Locate every blood parasite and identify its species.
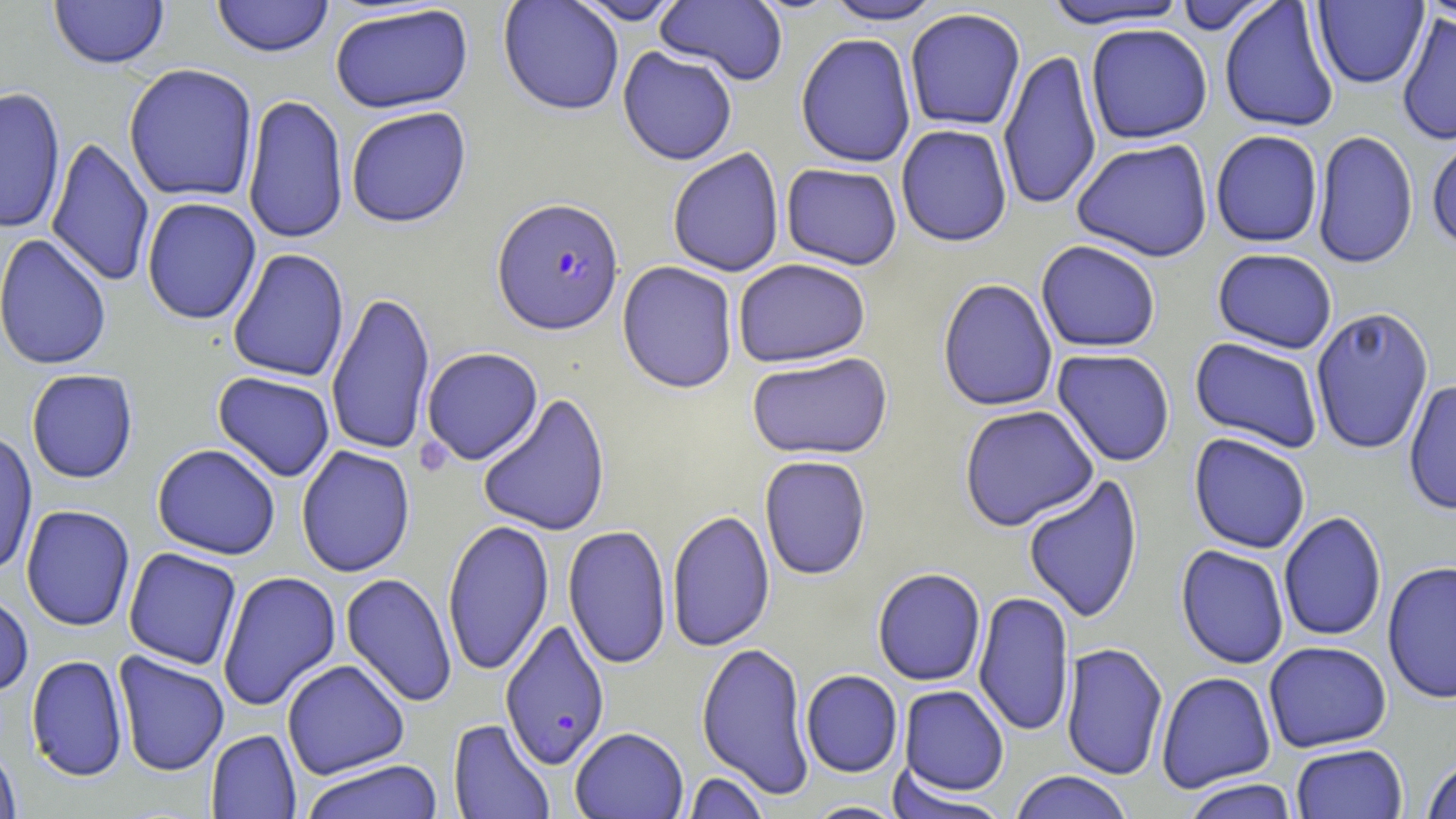
Approximate bounding boxes as (x1,y1)-(x2,y2) corner pairs in pixels.
Plasmodium falciparum-infected red blood cells: (492,196)-(624,336), (499,619)-(611,770).
No Plasmodium ovale, Plasmodium malariae, Plasmodium vivax, Babesia divergens, or Trypanosoma brucei observed.

slide-level diagnosis = Plasmodium falciparum
field of view = single
modality = optical microscopy
platelet locations = approximate bounding boxes as (x1,y1)-(x2,y2) corner pairs in pixels: (414,436)-(454,477)
stain = May-Grünwald-Giemsa
image size = 1456×819 pixels
uninfected red blood cell locations = approximate bounding boxes as (x1,y1)-(x2,y2) corner pairs in pixels: (48,0)-(170,70), (210,0)-(335,58), (498,0)-(624,116), (567,0)-(688,25), (655,0)-(790,86), (822,0)-(945,25), (1171,0)-(1280,34), (1417,0)-(1455,26), (1038,1)-(1191,30), (1219,1)-(1340,133), (1312,1)-(1429,89), (329,5)-(474,114), (904,8)-(1026,132), (1396,12)-(1456,146), (1085,23)-(1213,144), (795,32)-(917,168), (617,46)-(738,166), (998,48)-(1101,212), (123,63)-(258,204), (0,85)-(67,235), (242,94)-(349,245), (345,106)-(472,228), (896,124)-(1012,247), (1312,129)-(1419,269), (1210,130)-(1323,248), (1426,135)-(1456,250), (46,136)-(154,288), (1071,138)-(1213,263), (667,148)-(785,278), (780,163)-(903,270), (141,197)-(262,325), (0,233)-(113,370), (1035,240)-(1161,353), (227,248)-(349,382), (1212,248)-(1338,354), (732,258)-(871,368), (616,261)-(739,394), (937,278)-(1058,412), (326,290)-(435,457), (1310,306)-(1435,455), (1189,337)-(1324,453), (420,347)-(543,465), (1052,349)-(1175,467), (746,352)-(894,461), (25,369)-(139,484), (212,371)-(335,482), (1403,379)-(1456,516), (477,393)-(611,537), (959,405)-(1099,531), (0,428)-(38,578), (1188,433)-(1311,554), (152,443)-(281,560), (296,445)-(416,577), (759,455)-(871,580), (1022,474)-(1144,625), (20,505)-(136,632), (667,509)-(775,652), (1278,511)-(1387,642), (442,519)-(554,677), (562,524)-(672,669), (1175,545)-(1290,669), (123,547)-(242,670), (1381,560)-(1456,705), (872,568)-(986,686), (217,571)-(341,711), (340,572)-(458,708), (0,588)-(35,697), (973,591)-(1075,738), (1263,641)-(1392,752), (696,642)-(813,798), (1061,642)-(1169,781), (112,652)-(230,776), (25,654)-(129,782), (282,659)-(410,780), (801,670)-(903,778), (1156,671)-(1276,793), (898,685)-(1009,797), (447,718)-(555,818), (570,726)-(688,819), (206,729)-(301,819), (0,741)-(22,819), (1291,743)-(1408,818), (1420,758)-(1456,819), (299,759)-(445,819), (886,769)-(1007,818), (680,771)-(771,818), (1008,771)-(1134,819), (1181,778)-(1300,819), (801,801)-(909,818)
magnification = 1000x
preparation = thin blood smear